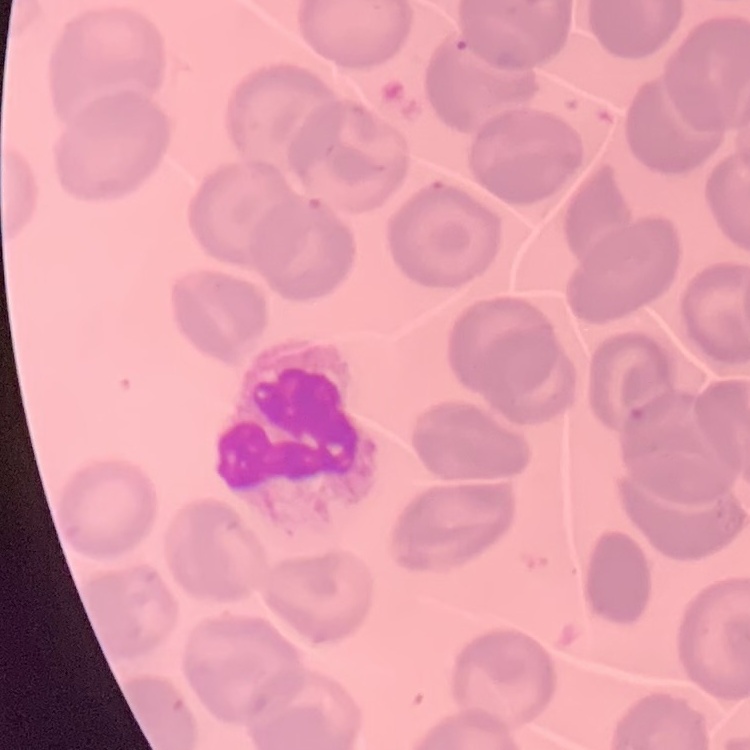

red_blood_cell_morphology: no rouleaux formation
preparation: thin blood film
stain: Field's or Giemsa
image_type: one tile cut from a larger photomicrograph